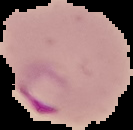
From a thin blood film. Result: Plasmodium parasites detected. The area outside the segmented cell region is set to black. Image is 133×130 pixels.